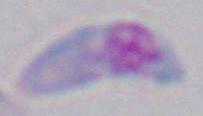

Summary:
  - Modality: micrograph
  - Identification: Toxoplasma gondii
  - Magnification: 1000x